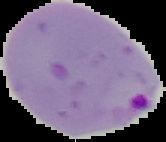
{
  "preparation": "thin blood smear",
  "image_type": "cell region segmented out of the field of view; surrounding area masked to black",
  "malaria_status": "parasitized",
  "image_size": "166×142 pixels"
}